Locate and identify every blood parasite.
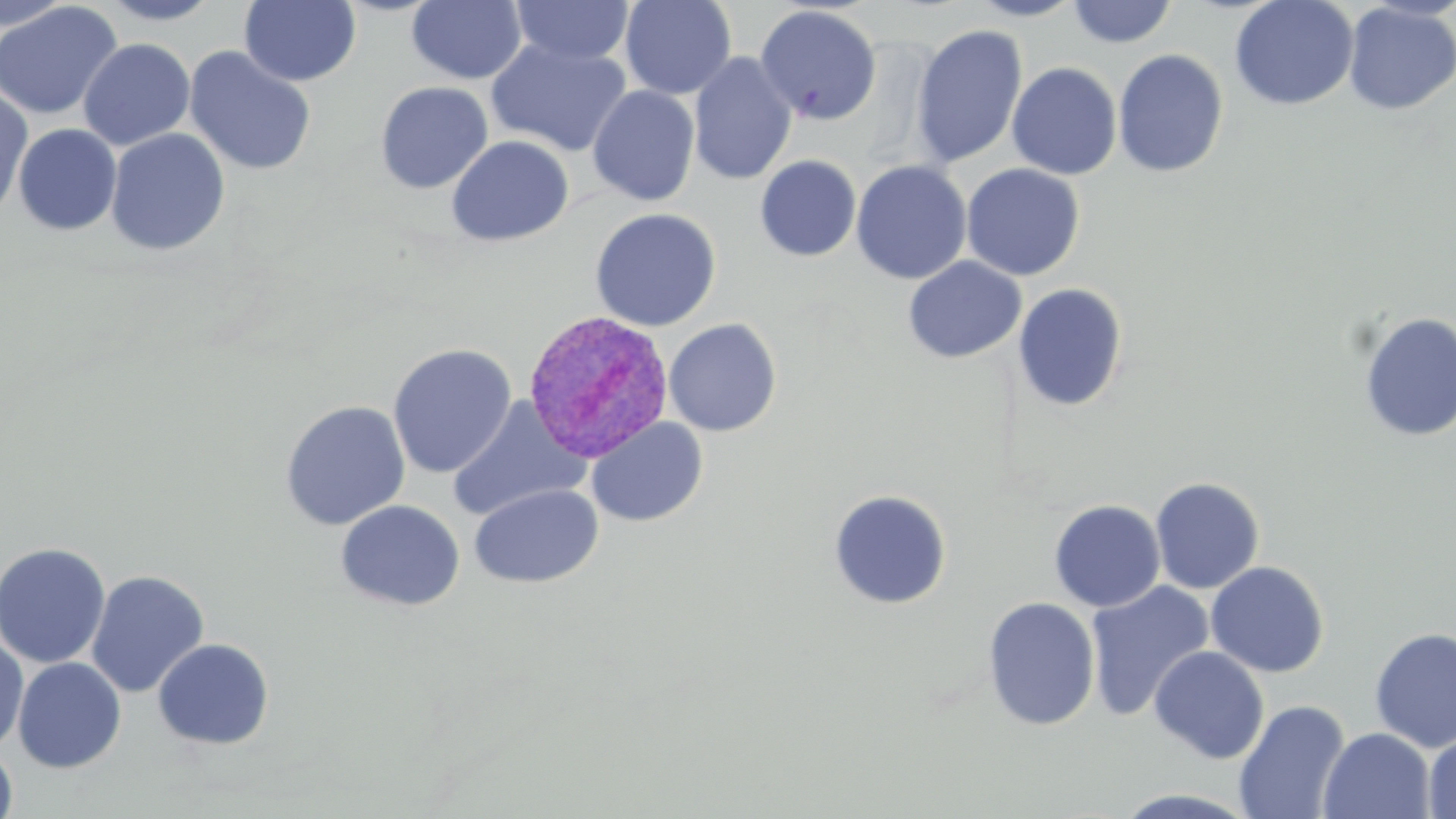
Approximate bounding boxes as (x1,y1)-(x2,y2) corner pairs in pixels.
Plasmodium vivax-infected red blood cells: (521,309)-(674,463).
No Plasmodium falciparum, Plasmodium ovale, Plasmodium malariae, Babesia divergens, or Trypanosoma brucei observed.

Summary:
  - Uninfected red blood cell locations: (98,0)-(224,25), (407,0)-(527,84), (619,0)-(737,100), (967,0)-(1085,21), (1229,0)-(1359,111), (0,1)-(75,33), (0,1)-(122,120), (239,1)-(362,87), (510,1)-(636,66), (1066,1)-(1178,48), (1342,2)-(1456,115), (754,5)-(882,126), (910,24)-(1028,168), (78,38)-(195,151), (486,38)-(632,156), (184,46)-(317,177), (1112,49)-(1229,178), (688,51)-(798,186), (1006,62)-(1122,180), (375,81)-(493,193), (586,85)-(700,207), (0,87)-(34,223), (12,124)-(122,235), (105,128)-(230,256), (446,135)-(575,246), (755,155)-(861,262), (850,160)-(972,284), (961,164)-(1085,281), (589,208)-(721,332), (903,256)-(1026,363), (1012,283)-(1128,412), (1357,312)-(1455,442), (663,318)-(783,436), (387,344)-(516,479), (446,398)-(590,522), (279,400)-(411,531), (586,417)-(708,528), (1150,476)-(1265,594), (469,483)-(602,589), (828,489)-(952,609), (1048,499)-(1166,612), (335,500)-(465,612), (0,541)-(111,669), (1205,561)-(1330,678), (85,569)-(210,698), (1085,581)-(1214,722), (983,596)-(1101,731), (1369,626)-(1456,753), (0,632)-(29,754), (152,638)-(275,750), (1149,645)-(1270,764), (12,657)-(127,773), (1234,700)-(1351,819), (1318,727)-(1436,818), (1423,730)-(1456,819), (0,743)-(18,819)
  - Slide-level diagnosis: Plasmodium vivax
  - Modality: optical microscopy
  - Image size: 1456×819 pixels
  - Preparation: thin blood smear
  - Magnification: 1000x
  - Stain: May-Grünwald-Giemsa
  - Field of view: one of a larger specimen